Assess the morphology of the erythrocytes.
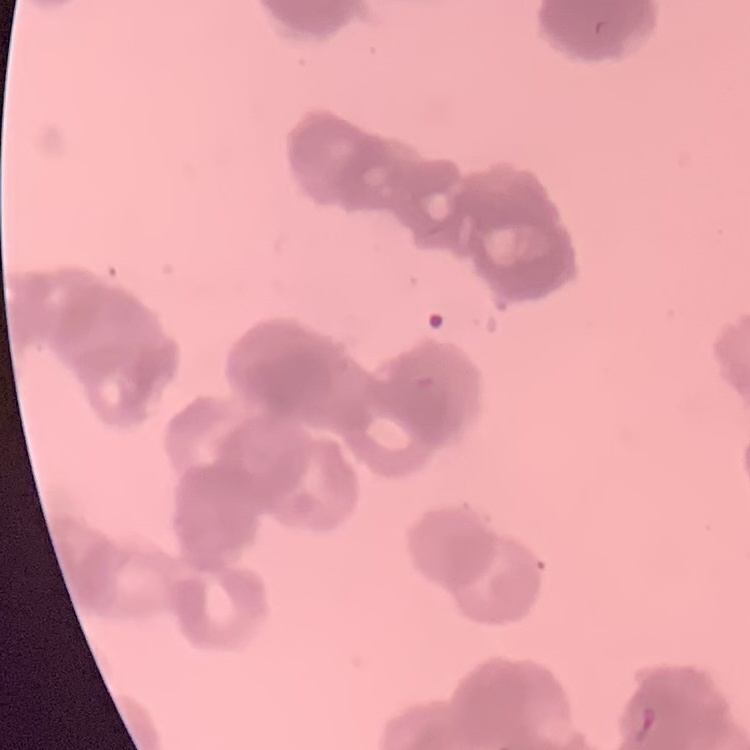
Rouleaux formation.

preparation = thin peripheral smear
image type = one tile cut from a larger photomicrograph
stain = Field's or Giemsa